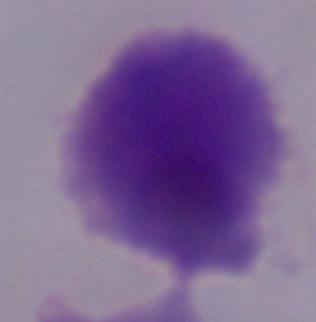
Summary:
  - Magnification: 1000x
  - Modality: micrograph
  - Identification: trichomonad